Assess the morphology of the red blood cells.
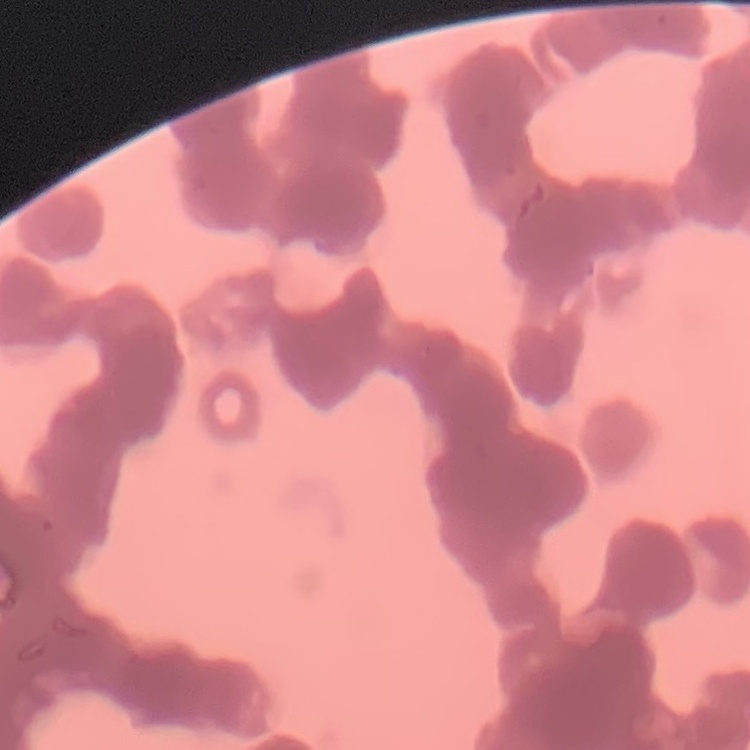

They show rouleaux formation.

Thin blood smear. Square crop of a larger photomicrograph. Field's or Giemsa stain.